Outline each blood parasite and name the species.
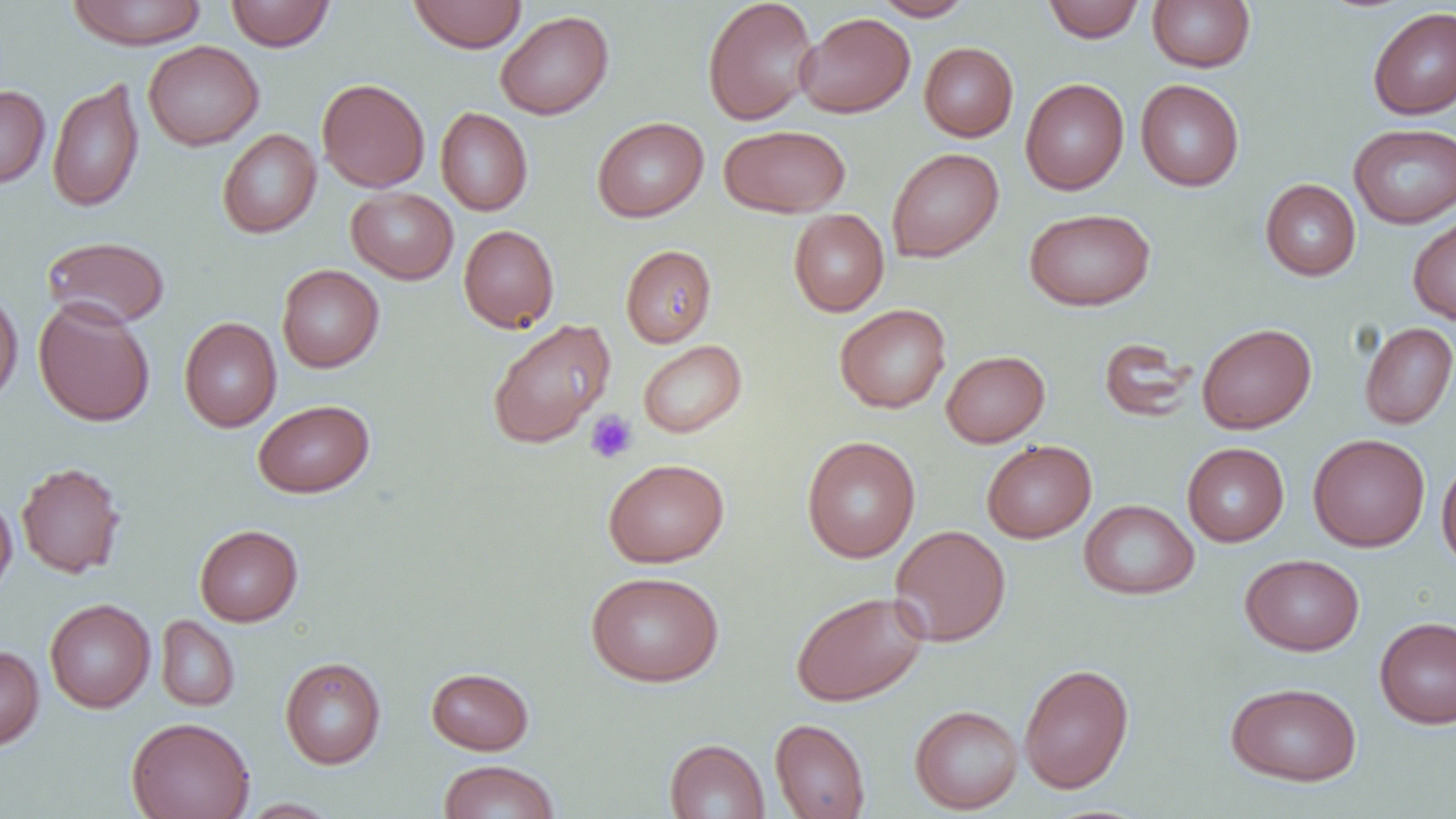

No blood parasites observed.

slide-level diagnosis = negative for blood parasites
preparation = thin blood smear
modality = optical microscopy
image size = 1456×819 pixels
platelet locations = approximate bounding boxes as [x1, y1, x2, y2] in pixels: [585, 410, 638, 463]
uninfected red blood cell locations = approximate bounding boxes as [x1, y1, x2, y2] in pixels: [66, 0, 208, 49], [225, 0, 336, 51], [407, 0, 527, 52], [702, 0, 819, 126], [871, 0, 974, 21], [1042, 0, 1145, 43], [1147, 0, 1256, 72], [1367, 6, 1456, 120], [495, 10, 614, 120], [795, 12, 915, 117], [143, 40, 264, 150], [919, 42, 1018, 141], [47, 78, 145, 213], [317, 78, 430, 193], [1020, 78, 1129, 195], [1135, 79, 1244, 191], [0, 84, 50, 189], [435, 107, 533, 216], [592, 116, 709, 222], [1348, 123, 1456, 228], [719, 124, 850, 218], [217, 129, 321, 238], [886, 147, 1003, 263], [1260, 179, 1361, 280], [346, 187, 458, 284], [1024, 208, 1155, 311], [788, 209, 889, 316], [1407, 213, 1456, 325], [459, 224, 559, 333], [41, 235, 170, 329], [621, 244, 717, 347], [276, 264, 384, 372], [0, 287, 23, 407], [33, 298, 156, 427], [834, 304, 951, 413], [179, 317, 282, 432], [487, 318, 616, 449], [1359, 322, 1456, 429], [1197, 323, 1316, 434], [1098, 337, 1197, 423], [638, 340, 747, 438], [941, 350, 1050, 447], [252, 399, 374, 498], [1308, 433, 1430, 552], [802, 435, 920, 563], [982, 439, 1096, 543], [1182, 442, 1289, 547], [1436, 456, 1456, 574], [603, 457, 730, 568], [16, 461, 126, 578], [0, 492, 17, 598], [1079, 499, 1199, 599], [195, 524, 303, 626], [890, 524, 1011, 646], [1240, 553, 1365, 655], [585, 571, 724, 687], [790, 590, 929, 706], [44, 598, 156, 713], [156, 615, 240, 711], [1374, 616, 1456, 729], [0, 645, 44, 750], [280, 656, 386, 769], [1018, 663, 1134, 794], [426, 667, 534, 755], [1225, 681, 1362, 786], [909, 705, 1024, 814], [126, 716, 255, 819], [770, 718, 870, 819], [664, 738, 769, 818], [437, 759, 560, 818], [238, 798, 342, 818]
magnification = 1000x
field of view = single